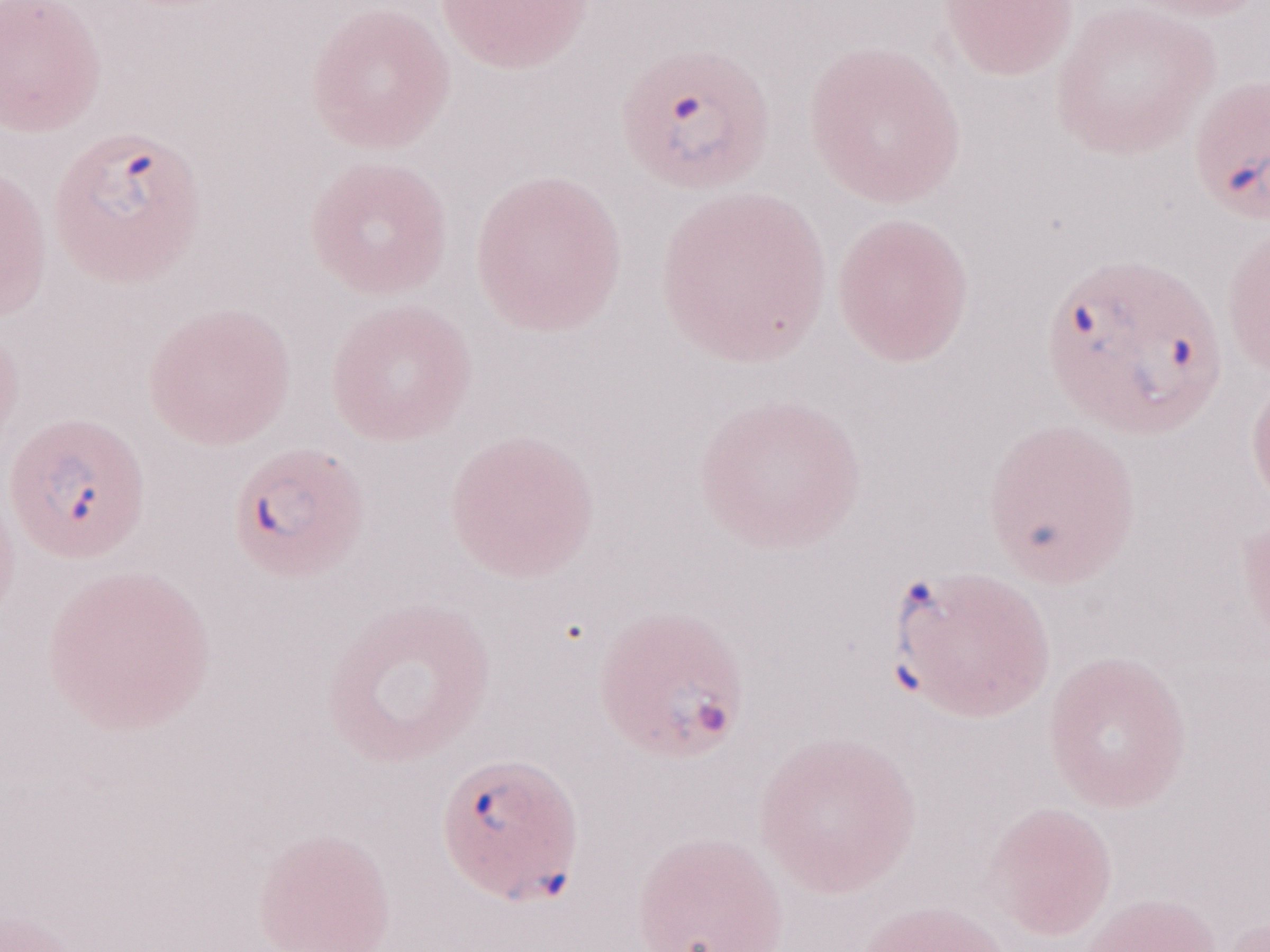
May-Grünwald-Giemsa stain. Olympus BX43 microscope, Olympus DP73 camera. One field of this slide. Magnification: 1,000x. Thin peripheral-blood smear. Image is 1270×952 pixels. Patient-level malaria diagnosis: positive.